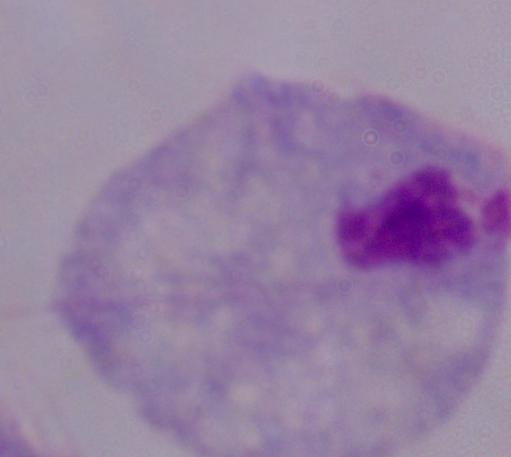

Captured at 1000x magnification. A trichomonad is shown. Photomicrograph.